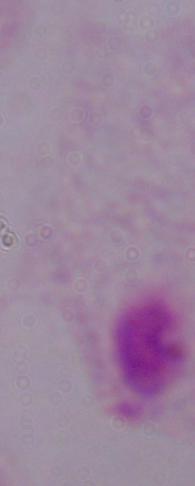

Summary:
  - Magnification: 1000x
  - Modality: photomicrograph
  - Identification: trichomonad